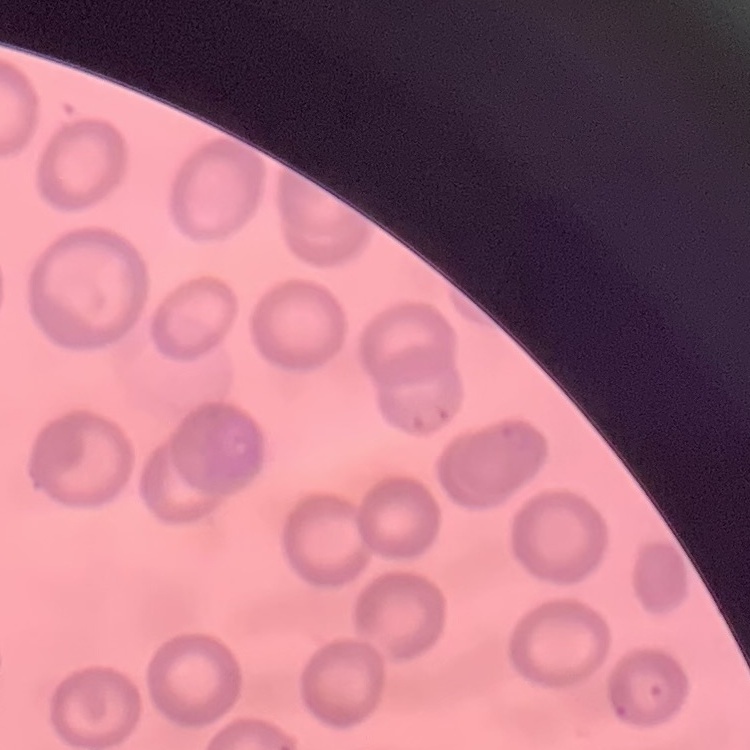

Summary:
  - Erythrocyte morphology: no rouleaux formation
  - Image type: one tile cut from a larger photomicrograph
  - Preparation: thin peripheral smear
  - Stain: Field's or Giemsa